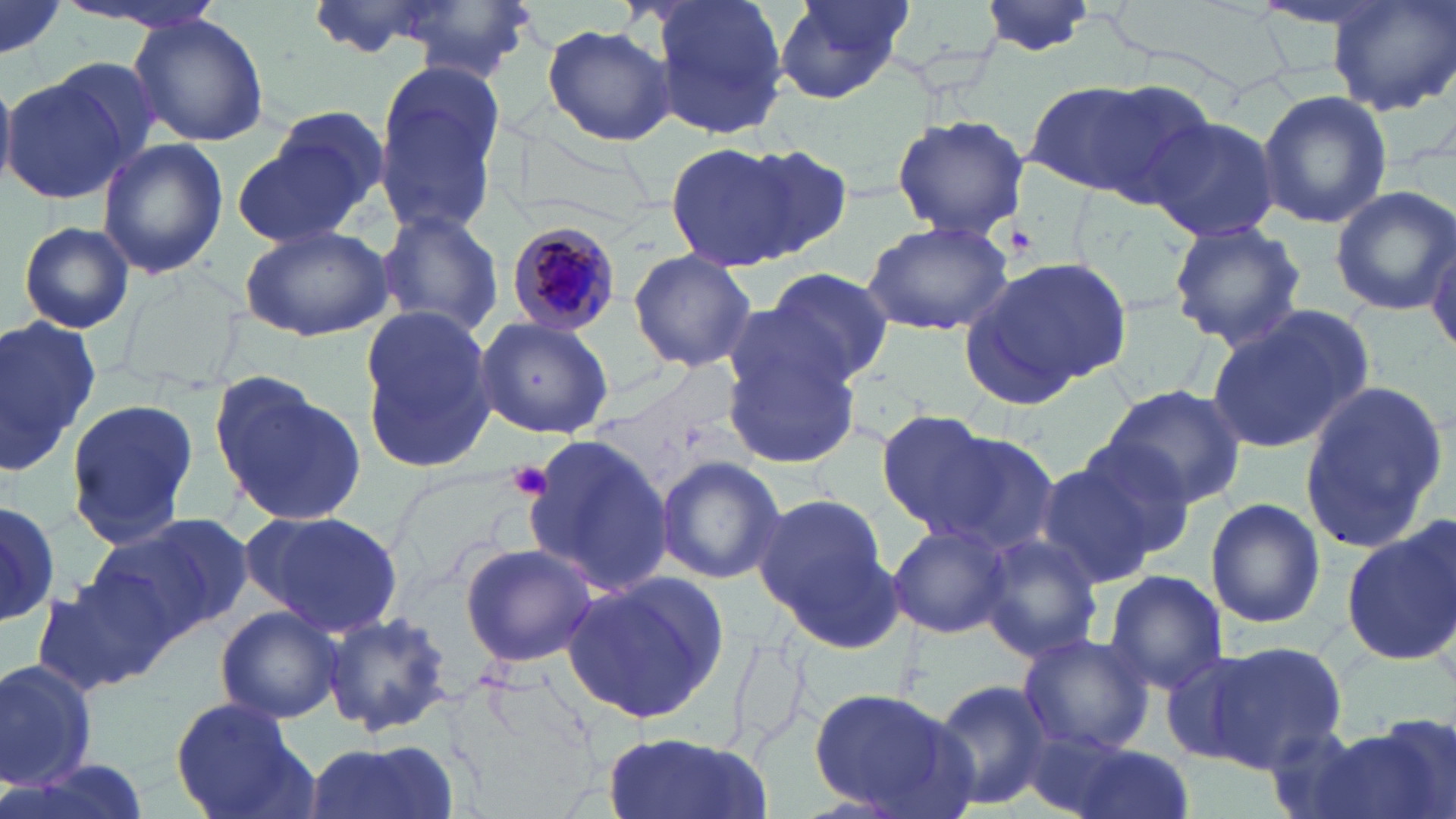

Approximate bounding boxes as (x1,y1)-(x2,y2) corner pairs in pixels. Plasmodium malariae-infected red blood cell locations: (505,219)-(620,336). Platelet locations: (507,459)-(554,500). Uninfected red blood cell locations: (60,0)-(230,33), (383,0)-(545,80), (648,0)-(792,139), (770,0)-(915,105), (1249,0)-(1414,33), (1327,0)-(1456,116), (979,1)-(1099,56), (0,2)-(66,65), (128,15)-(269,145), (542,23)-(673,145), (371,59)-(508,240), (1,72)-(134,206), (1029,77)-(1202,203), (1257,89)-(1393,229), (890,114)-(1029,243), (1148,116)-(1282,244), (229,127)-(375,249), (97,137)-(229,280), (664,141)-(810,272), (740,144)-(853,257), (1329,183)-(1454,318), (372,209)-(506,339), (862,218)-(1013,334), (1167,219)-(1307,352), (17,220)-(136,334), (239,225)-(393,343), (1427,235)-(1455,365), (627,249)-(757,372), (957,255)-(1133,406), (765,267)-(894,387), (359,307)-(496,471), (1205,308)-(1370,454), (0,313)-(101,474), (474,318)-(613,440), (722,344)-(864,468), (210,373)-(367,530), (1299,378)-(1453,555), (1098,384)-(1247,508), (64,397)-(204,551), (875,409)-(996,531), (919,428)-(1062,557), (519,433)-(672,599), (1065,434)-(1204,560), (655,454)-(786,585), (1035,459)-(1160,589), (753,490)-(896,635), (1205,496)-(1325,629), (0,501)-(60,628), (244,509)-(403,640), (88,515)-(247,644), (886,521)-(1010,640), (1341,522)-(1456,667), (978,534)-(1103,662), (459,542)-(598,668), (1100,570)-(1228,694), (30,571)-(170,698), (564,575)-(728,725), (215,606)-(342,722), (323,611)-(455,739), (1015,631)-(1156,752), (1203,641)-(1347,771), (1157,651)-(1264,764), (0,658)-(100,791), (932,677)-(1056,810), (807,688)-(975,818), (170,697)-(315,819), (1339,717)-(1455,819), (1260,725)-(1393,819), (599,732)-(771,819), (299,738)-(451,819), (1046,741)-(1194,819). Slide-level diagnosis: Plasmodium malariae. May-Grünwald-Giemsa stain. Light microscopy. Thin blood smear. Image is 1456×819 pixels. One field of a larger specimen. 1000x magnification.